Identify the parasite.
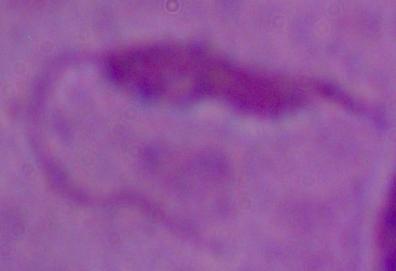
This is Leishmania.

Photomicrograph. Captured at 1000x magnification.